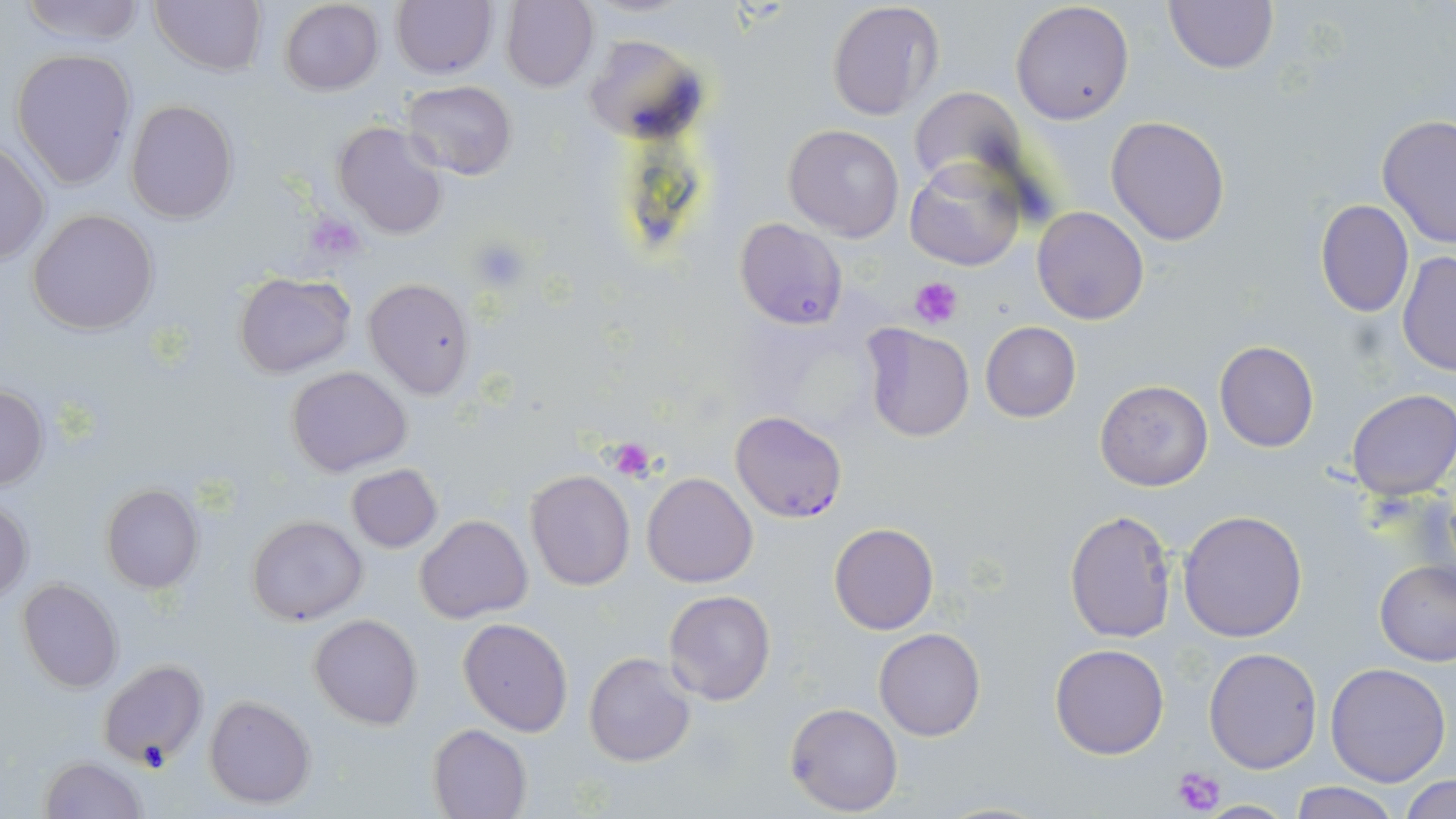
{
  "slide_level_diagnosis": "Plasmodium falciparum",
  "uninfected_red_blood_cell_locations": "approximate bounding boxes as [x1, y1, x2, y2] in pixels: [15, 0, 149, 48], [149, 0, 268, 77], [501, 0, 598, 92], [1163, 0, 1278, 73], [279, 1, 383, 96], [390, 1, 496, 78], [825, 2, 942, 120], [1011, 2, 1135, 125], [583, 34, 706, 143], [10, 50, 135, 190], [401, 80, 518, 182], [906, 86, 1025, 198], [126, 99, 238, 224], [1105, 115, 1231, 248], [1375, 115, 1456, 249], [331, 120, 450, 240], [783, 124, 905, 242], [0, 142, 48, 267], [906, 157, 1026, 272], [1314, 198, 1414, 317], [1031, 206, 1150, 326], [28, 208, 159, 334], [734, 217, 848, 331], [1397, 251, 1455, 376], [235, 272, 354, 379], [363, 277, 476, 399], [980, 321, 1080, 422], [859, 322, 974, 442], [1214, 341, 1320, 452], [288, 365, 412, 478], [1094, 379, 1213, 492], [1, 386, 48, 489], [1345, 390, 1456, 500], [346, 464, 442, 552], [525, 469, 634, 591], [643, 473, 756, 587], [99, 483, 203, 593], [1, 497, 33, 600], [1064, 509, 1178, 645], [1177, 510, 1307, 643], [246, 513, 368, 625], [415, 515, 532, 623], [828, 523, 939, 634], [1375, 561, 1456, 666], [17, 579, 123, 693], [663, 589, 777, 705], [309, 614, 422, 729], [458, 617, 573, 738], [874, 627, 985, 741], [1050, 643, 1169, 758], [1203, 647, 1322, 773], [583, 652, 697, 767], [97, 657, 206, 766], [1325, 663, 1450, 786], [204, 695, 316, 808], [785, 702, 903, 815], [427, 723, 531, 819], [39, 755, 148, 819], [1401, 775, 1456, 818], [1288, 781, 1401, 818], [1198, 799, 1295, 817]",
  "platelet_locations": "approximate bounding boxes as [x1, y1, x2, y2] in pixels: [471, 237, 530, 292], [911, 276, 962, 328], [608, 439, 660, 480], [1169, 764, 1227, 817]",
  "preparation": "thin blood smear",
  "plasmodium_falciparum_infected_red_blood_cell_locations": "approximate bounding boxes as [x1, y1, x2, y2] in pixels: [729, 410, 850, 519]",
  "field_of_view": "single",
  "modality": "light microscopy",
  "stain": "May-Grünwald-Giemsa",
  "magnification": "1000x",
  "image_size": "1456×819 pixels"
}